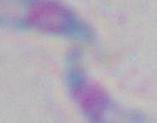
Toxoplasma gondii is seen. Photomicrograph. Captured at 1000x magnification.